Report the malaria status of this cell.
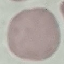
Uninfected.

capture = smartphone camera at the microscope eyepiece
preparation = thin smear
stain = Giemsa
image type = cell patch, automatically extracted from a larger field of view and resized to 64 × 64 pixels